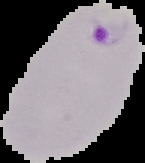
{
  "image_size": "145×163 pixels",
  "image_type": "segmented cell region on a black background",
  "preparation": "thin blood smear",
  "malaria_status": "parasitized"
}